Classify this cell by malaria status.
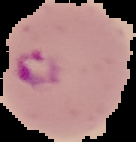
Parasitized.

image_size: 136×142 pixels
image_type: segmented cell region on a black background
preparation: thin blood film